Describe the morphology of the red blood cells.
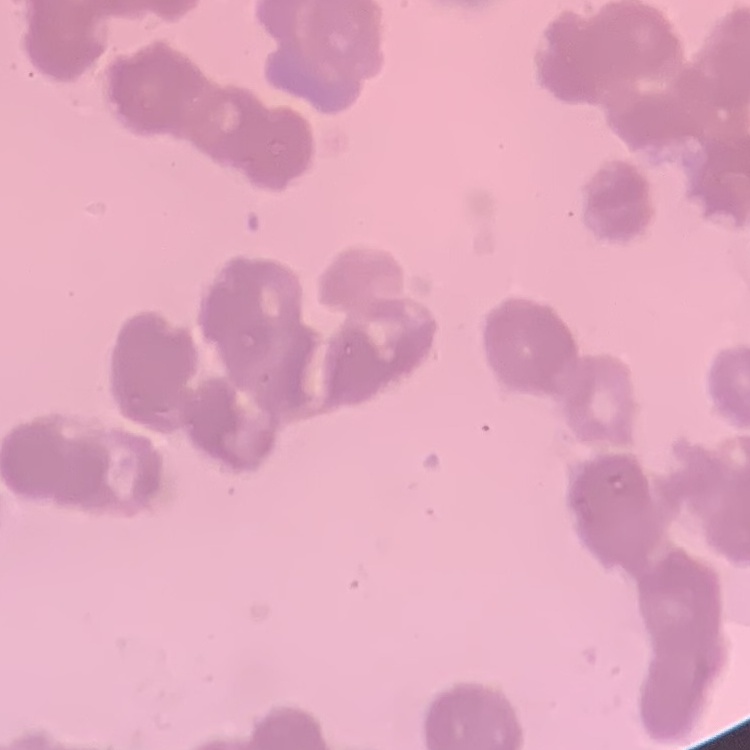

Rouleaux formation.

{
  "image_type": "one tile cut from a larger photomicrograph",
  "preparation": "thin blood film",
  "stain": "Field's or Giemsa"
}